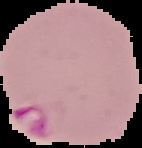
malaria status = parasitized
image size = 142×148 pixels
preparation = thin blood film
image type = cell region segmented out of the field of view; surrounding area masked to black